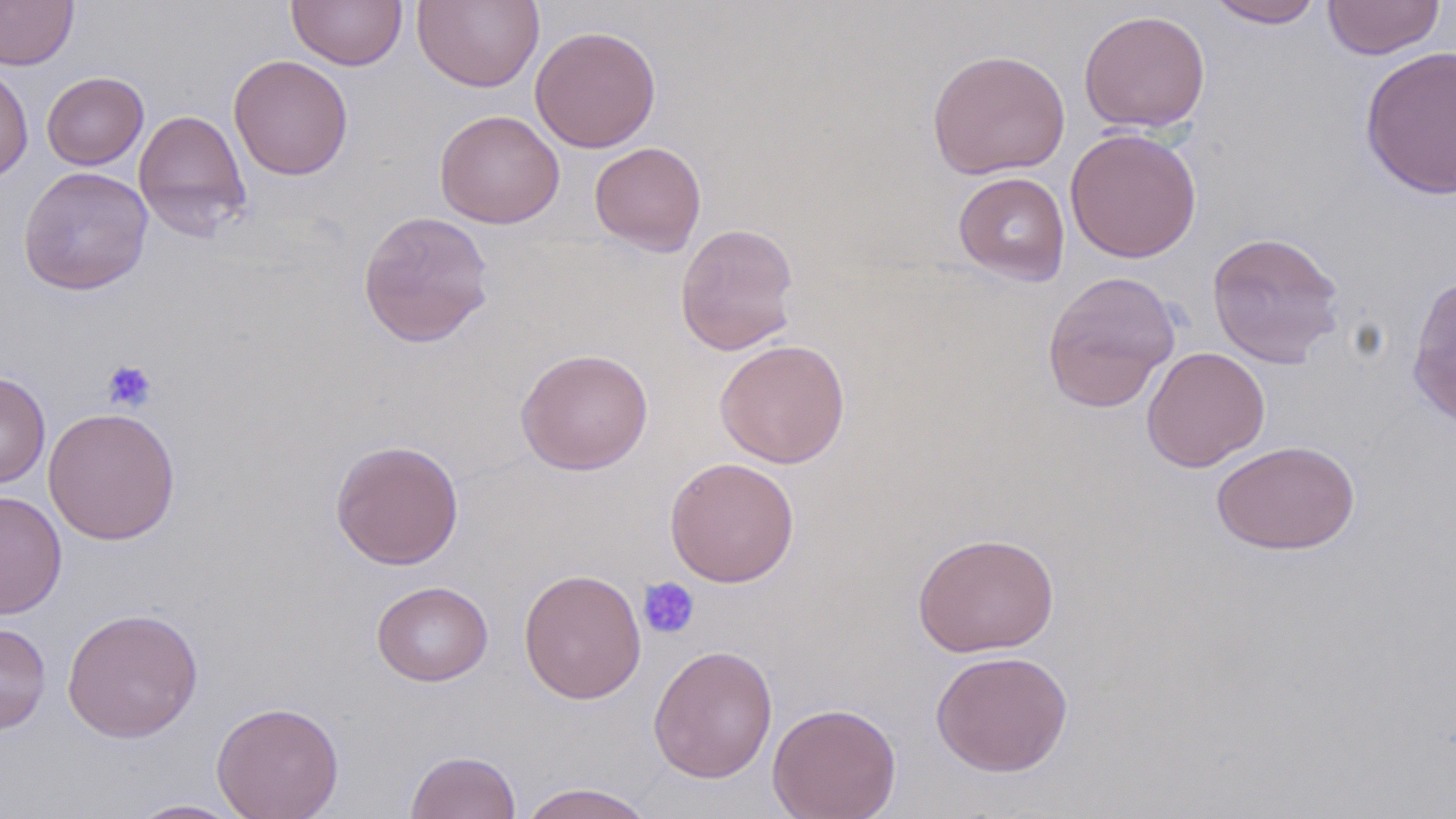
Approximate bounding boxes as [x1, y1, x2, y2] in pixels. Uninfected red blood cell locations: [0, 0, 79, 70], [413, 0, 544, 92], [1206, 0, 1326, 28], [1322, 0, 1446, 60], [286, 1, 408, 70], [1079, 8, 1211, 133], [530, 25, 661, 153], [1360, 45, 1456, 200], [927, 48, 1070, 179], [228, 54, 354, 181], [0, 63, 34, 185], [42, 71, 148, 170], [133, 109, 252, 241], [434, 109, 565, 229], [1064, 127, 1202, 264], [589, 141, 706, 256], [18, 166, 154, 294], [953, 171, 1071, 286], [357, 210, 495, 348], [675, 222, 800, 356], [1206, 231, 1346, 368], [1041, 270, 1181, 413], [1407, 271, 1456, 430], [714, 339, 850, 469], [1141, 346, 1270, 472], [515, 348, 654, 475], [0, 371, 51, 489], [43, 407, 181, 546], [330, 439, 465, 569], [1211, 439, 1360, 555], [664, 456, 800, 587], [0, 490, 67, 620], [913, 532, 1060, 657], [518, 568, 647, 704], [371, 580, 493, 686], [62, 606, 203, 743], [0, 621, 51, 734], [647, 644, 778, 783], [930, 649, 1074, 777], [211, 701, 344, 819], [767, 702, 902, 819], [404, 750, 521, 819], [517, 782, 658, 819], [125, 798, 249, 818]. Platelet locations: [101, 359, 157, 413], [637, 577, 700, 639]. Slide-level diagnosis: no evidence of blood parasites. Single field of view. Thin blood film. Captured at 1000x magnification. Image is 1456×819 pixels. Optical microscopy. May-Grünwald-Giemsa stain.